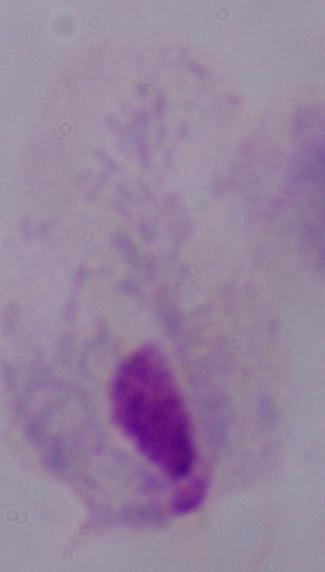 Micrograph. Captured at 1000x magnification. A trichomonad is shown.